Locate every blood parasite and identify its species.
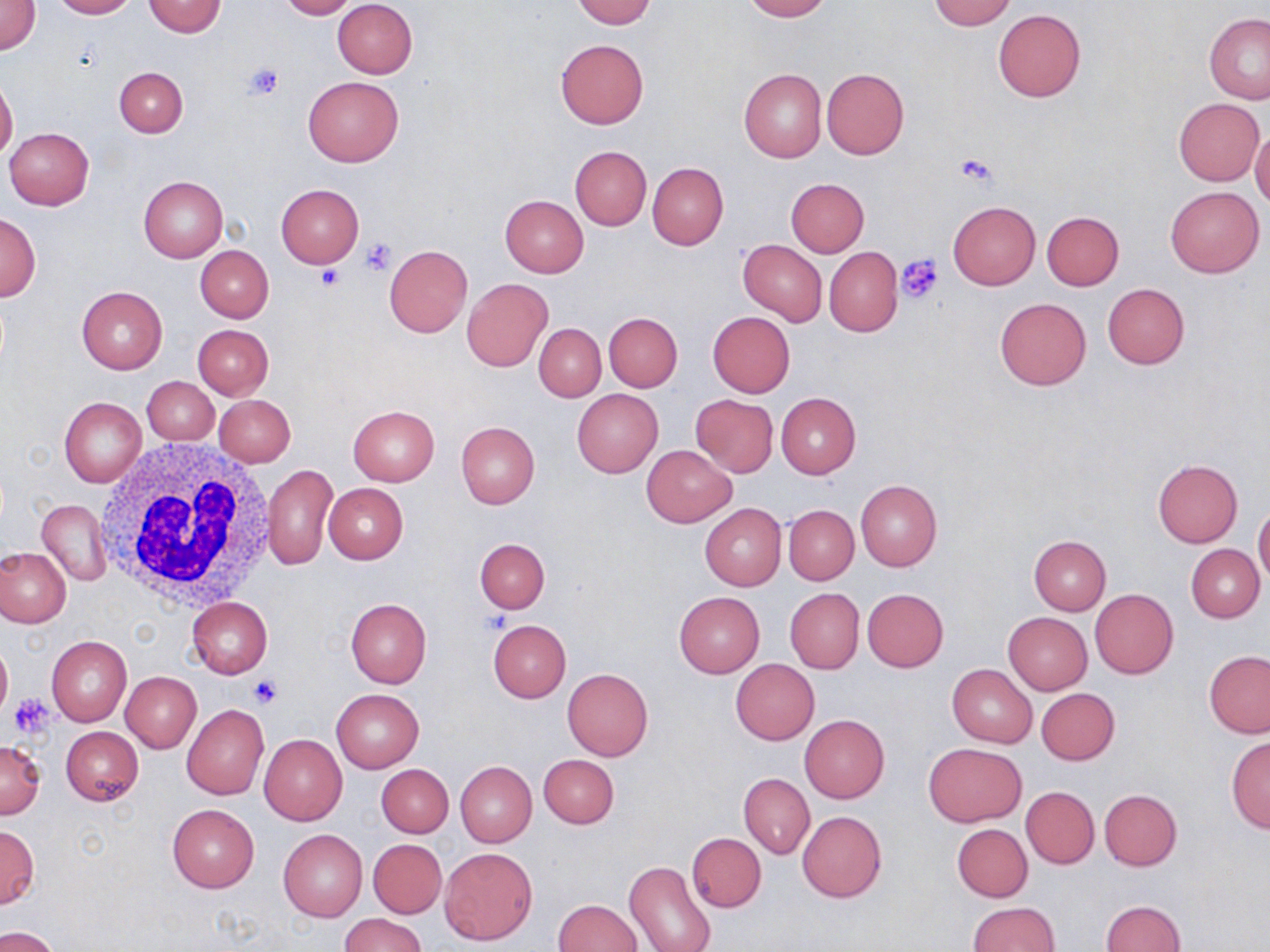

No blood parasites observed.

Summary:
  - Coordinate format: approximate bounding boxes as (x1,y1)-(x2,y2) corner pairs in pixels
  - White blood cell locations: (95,436)-(278,612)
  - Uninfected red blood cell locations: (0,0)-(41,55), (52,0)-(136,19), (278,0)-(356,19), (333,0)-(417,78), (572,0)-(655,26), (741,0)-(831,20), (929,0)-(1016,30), (142,1)-(227,37), (992,9)-(1086,102), (1203,13)-(1270,104), (1191,15)-(1266,183), (555,39)-(649,129), (115,66)-(187,136), (738,68)-(825,163), (821,68)-(908,159), (303,76)-(404,167), (0,78)-(18,161), (1173,98)-(1264,186), (4,127)-(94,210), (1250,129)-(1270,209), (570,146)-(651,229), (647,161)-(728,249), (138,175)-(228,262), (785,178)-(869,257), (276,183)-(365,267), (1164,184)-(1264,278), (500,194)-(588,277), (948,200)-(1040,289), (1041,211)-(1124,289), (1,212)-(41,302), (739,241)-(827,325), (384,244)-(473,337), (195,245)-(273,322), (824,246)-(903,336), (462,278)-(553,372), (1102,283)-(1190,369), (77,285)-(168,373), (994,297)-(1092,390), (604,312)-(682,391), (707,312)-(795,397), (535,323)-(605,402), (193,324)-(274,400), (142,377)-(219,444), (572,388)-(663,476), (776,392)-(860,478), (214,395)-(295,468), (691,395)-(778,476), (58,397)-(146,486), (347,405)-(440,485), (455,421)-(539,509), (641,445)-(736,527), (1152,459)-(1243,547), (262,463)-(336,571), (855,480)-(942,571), (323,483)-(408,564), (36,499)-(111,586), (700,503)-(786,591), (1253,504)-(1270,586), (784,505)-(858,585), (1028,535)-(1110,616), (476,537)-(550,613), (1187,545)-(1265,622), (0,547)-(71,627), (1090,588)-(1178,678), (784,589)-(864,674), (862,589)-(949,672), (674,592)-(765,677), (187,597)-(272,678), (345,597)-(432,687), (1004,613)-(1092,695), (487,619)-(571,703), (47,636)-(131,727), (0,643)-(12,723), (1204,651)-(1270,738), (731,658)-(819,745), (947,663)-(1037,748), (562,668)-(653,761), (121,672)-(201,753), (331,688)-(424,773), (1036,688)-(1120,765), (181,704)-(268,799), (800,715)-(889,803), (61,726)-(143,806), (259,734)-(347,825), (1225,737)-(1270,833), (0,739)-(46,819), (923,743)-(1027,827), (538,754)-(619,829), (455,761)-(537,847), (376,763)-(453,838), (739,773)-(814,859), (1021,787)-(1098,868), (1099,789)-(1181,871), (167,804)-(259,893), (797,811)-(887,902), (952,822)-(1033,902), (0,823)-(38,909), (278,829)-(367,922), (687,832)-(765,912), (369,839)-(446,918), (441,847)-(537,945), (624,860)-(715,952), (552,900)-(642,951), (1100,900)-(1185,952), (966,902)-(1059,952), (341,913)-(425,952), (0,926)-(61,952)
  - Platelet locations: (244,63)-(285,101), (954,153)-(1001,190), (361,237)-(396,274), (895,255)-(943,303), (315,264)-(345,290), (250,676)-(282,708), (8,694)-(55,740)
  - Slide-level diagnosis: no evidence of blood parasites
  - Preparation: thin blood film
  - Stain: May-Grünwald-Giemsa
  - Magnification: 1000x
  - Image size: 1270×952 pixels
  - Field of view: one of a larger specimen
  - Modality: optical microscopy